Report the malaria status of this cell.
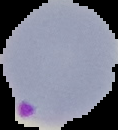
It is parasitized.

image size = 118×130 pixels
image type = segmented cell region with the area outside set to black
preparation = thin blood film